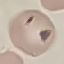
Summary:
  - Result: no malaria parasites seen
  - Image type: automatically extracted cell patch, resized to 64 × 64 pixels
  - Preparation: thin smear
  - Capture: smartphone camera at the microscope eyepiece
  - Stain: Giemsa